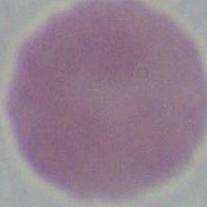

magnification: 1000x
modality: micrograph
identification: erythrocyte